Identify the parasite.
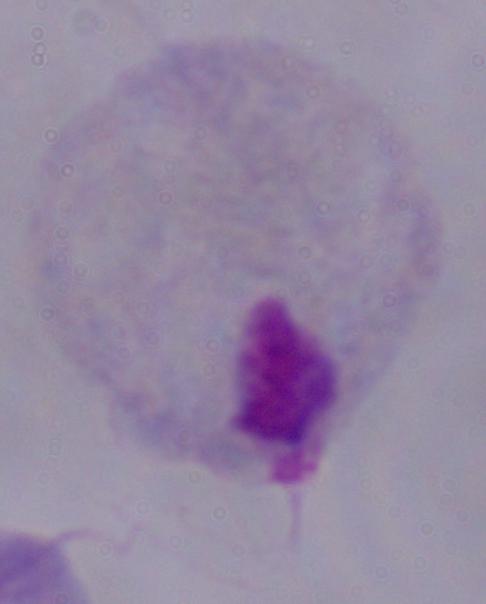
A trichomonad.

magnification = 1000x
modality = photomicrograph